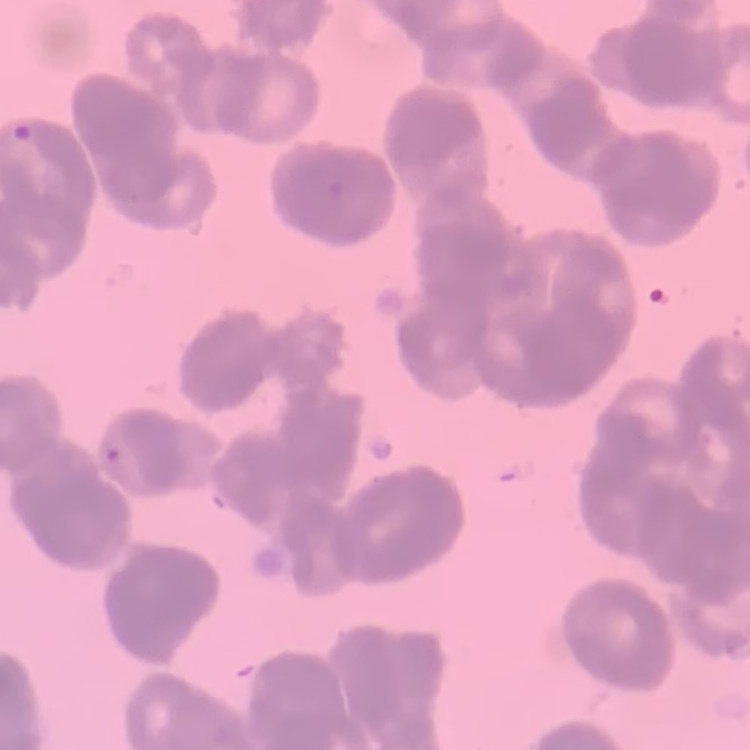
erythrocyte morphology = rouleaux formation
preparation = thin blood film
image type = square crop of a larger photomicrograph
stain = Field's or Giemsa